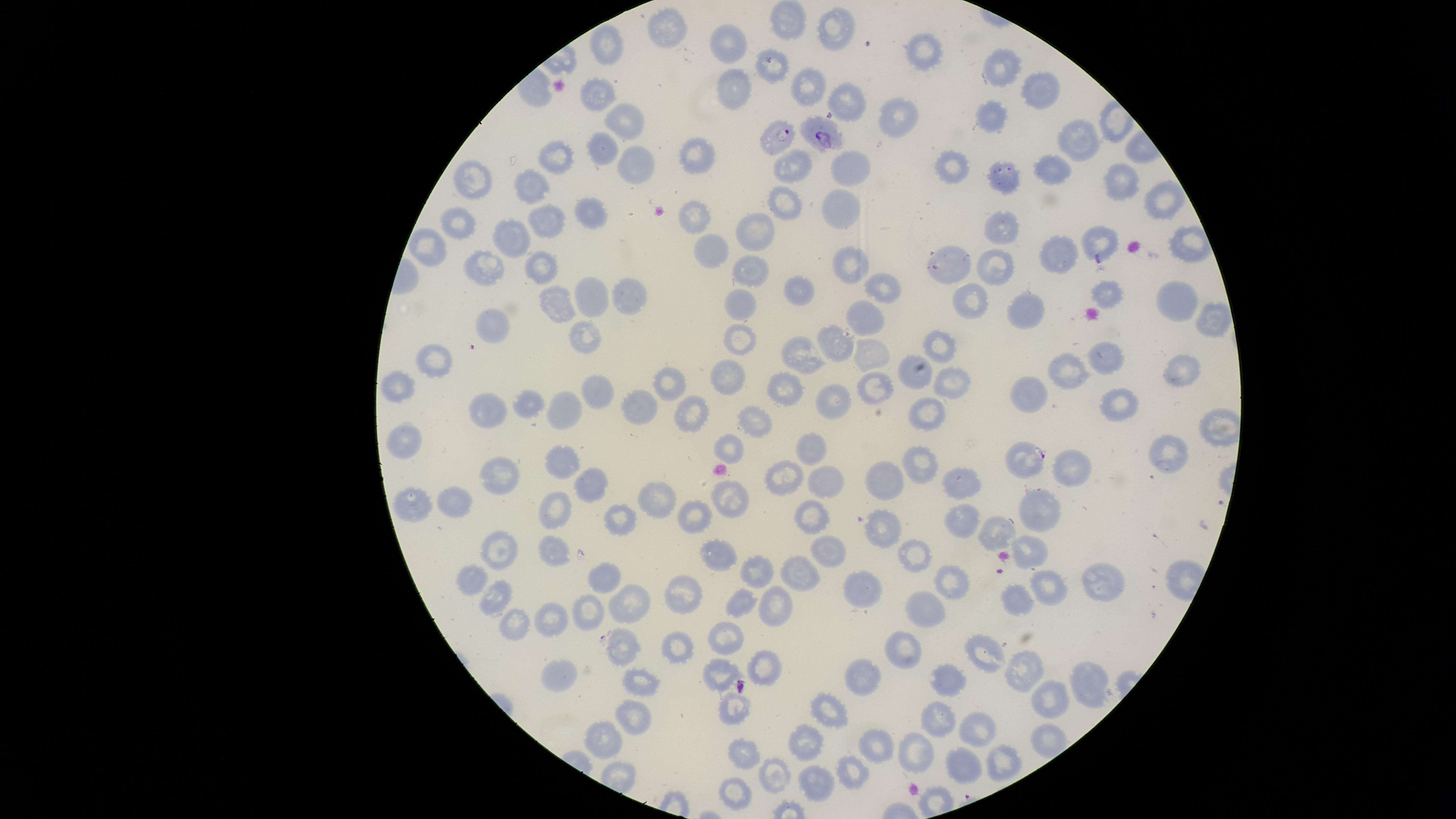
Approximate marker points as {x, y} in pixels.
Summary:
  - Parasitized red blood cells: {778, 137}, {826, 138}, {1028, 461}
  - Uninfected red blood cells: {781, 20}, {664, 28}, {829, 30}, {730, 41}, {606, 47}, {921, 53}, {772, 61}, {999, 68}, {812, 85}, {730, 91}, {593, 92}, {1038, 93}, {846, 101}, {887, 113}, {630, 115}, {994, 120}, {1075, 140}, {598, 149}, {638, 153}, {689, 154}, {556, 159}, {792, 164}, {842, 164}, {954, 169}, {1052, 170}, {1000, 178}, {471, 183}, {537, 184}, {1116, 184}, {1162, 199}, {837, 202}, {787, 203}, {694, 215}, {588, 217}, {461, 224}, {1000, 226}, {549, 227}, {756, 232}, {1096, 239}, {511, 240}, {429, 251}, {707, 251}, {1050, 256}, {951, 262}, {849, 263}, {484, 264}, {538, 265}, {993, 266}, {753, 269}, {881, 283}, {794, 289}, {593, 292}, {625, 293}, {1102, 296}, {552, 302}, {1172, 302}, {970, 304}, {741, 305}, {1020, 310}, {863, 318}, {1202, 319}, {494, 326}, {587, 331}, {833, 345}, {940, 346}, {742, 347}, {867, 351}, {435, 353}, {798, 355}, {1099, 357}, {1181, 366}, {1069, 370}, {727, 374}, {921, 378}, {880, 380}, {953, 380}, {1032, 383}, {596, 384}, {784, 384}, {403, 386}, {669, 387}, {831, 394}, {1120, 400}, {532, 403}, {645, 405}, {923, 407}, {559, 408}, {485, 409}, {693, 413}, {748, 421}, {725, 442}, {403, 446}, {1163, 449}, {808, 452}, {917, 463}, {562, 465}, {1069, 472}, {785, 475}, {498, 476}, {827, 478}, {888, 481}, {956, 484}, {593, 486}, {737, 496}, {660, 499}, {458, 504}, {410, 507}, {1038, 507}, {554, 513}, {961, 515}, {700, 516}, {810, 516}, {615, 520}, {996, 531}, {876, 532}, {822, 548}, {500, 549}, {1028, 551}, {554, 555}, {719, 556}, {910, 556}, {757, 572}, {799, 575}, {603, 576}, {942, 577}, {1090, 578}, {475, 581}, {1048, 583}, {855, 588}, {495, 594}, {684, 596}, {741, 596}, {1014, 598}, {624, 599}, {773, 599}, {920, 606}, {588, 610}, {512, 619}, {552, 620}, {729, 635}, {625, 650}, {676, 650}, {896, 650}, {984, 655}, {1026, 667}, {767, 669}, {719, 673}, {857, 674}, {640, 675}, {949, 679}, {1086, 679}, {560, 684}, {1047, 695}, {732, 705}, {826, 708}, {632, 713}, {938, 721}, {979, 731}, {604, 738}, {805, 743}, {879, 745}, {735, 756}, {915, 757}, {1000, 759}, {959, 767}, {770, 771}, {851, 777}, {822, 792}, {730, 798}
  - Species: Plasmodium falciparum
  - Visible region: circular
  - Image size: 1456×819 pixels
  - Capture: smartphone photograph through the microscope eyepiece
  - Presence: malaria parasites seen
  - Preparation: thin blood film
  - Stain: Giemsa
  - Field of view: single